Classify this cell by malaria status.
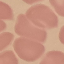

Uninfected.

Summary:
  - Preparation: thin blood smear
  - Capture: smartphone through the microscope eyepiece
  - Stain: Giemsa
  - Image type: cell patch, automatically extracted from a larger field of view and resized to 64 × 64 pixels